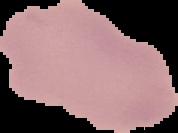
image_size: 178×133 pixels
image_type: segmented cell region on a black background
malaria_status: uninfected
preparation: thin blood smear